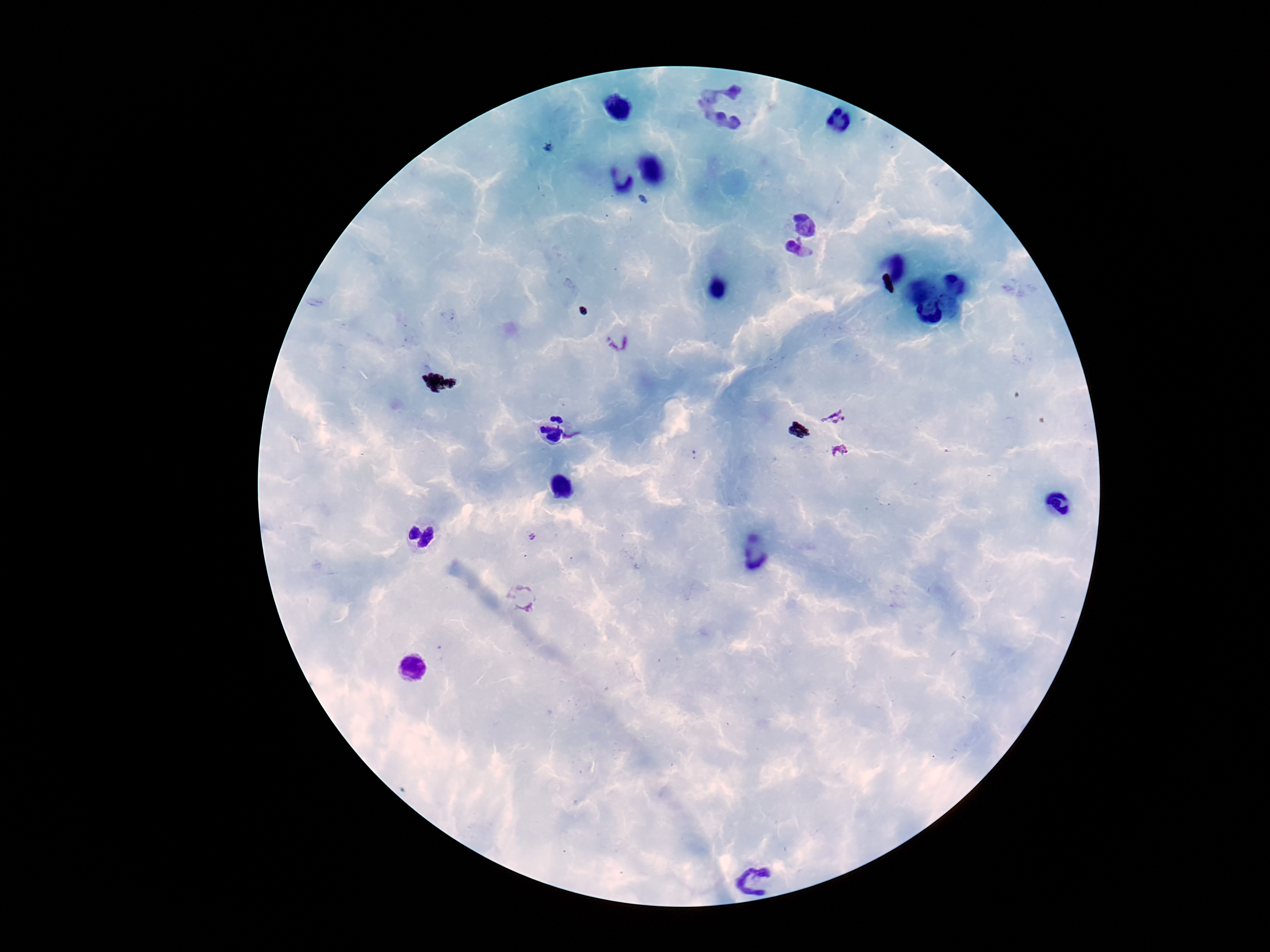 Approximate centers as [x, y] in pixels. Plasmodium parasite locations: [619, 342], [833, 416], [841, 453], [521, 598]. Single field of view. Giemsa-stained preparation. Photographed through the microscope eyepiece with a smartphone camera. Thick peripheral-blood smear. Image is 1270×952 pixels. Patient malaria status: positive. 100x magnification.